Locate every Plasmodium parasite.
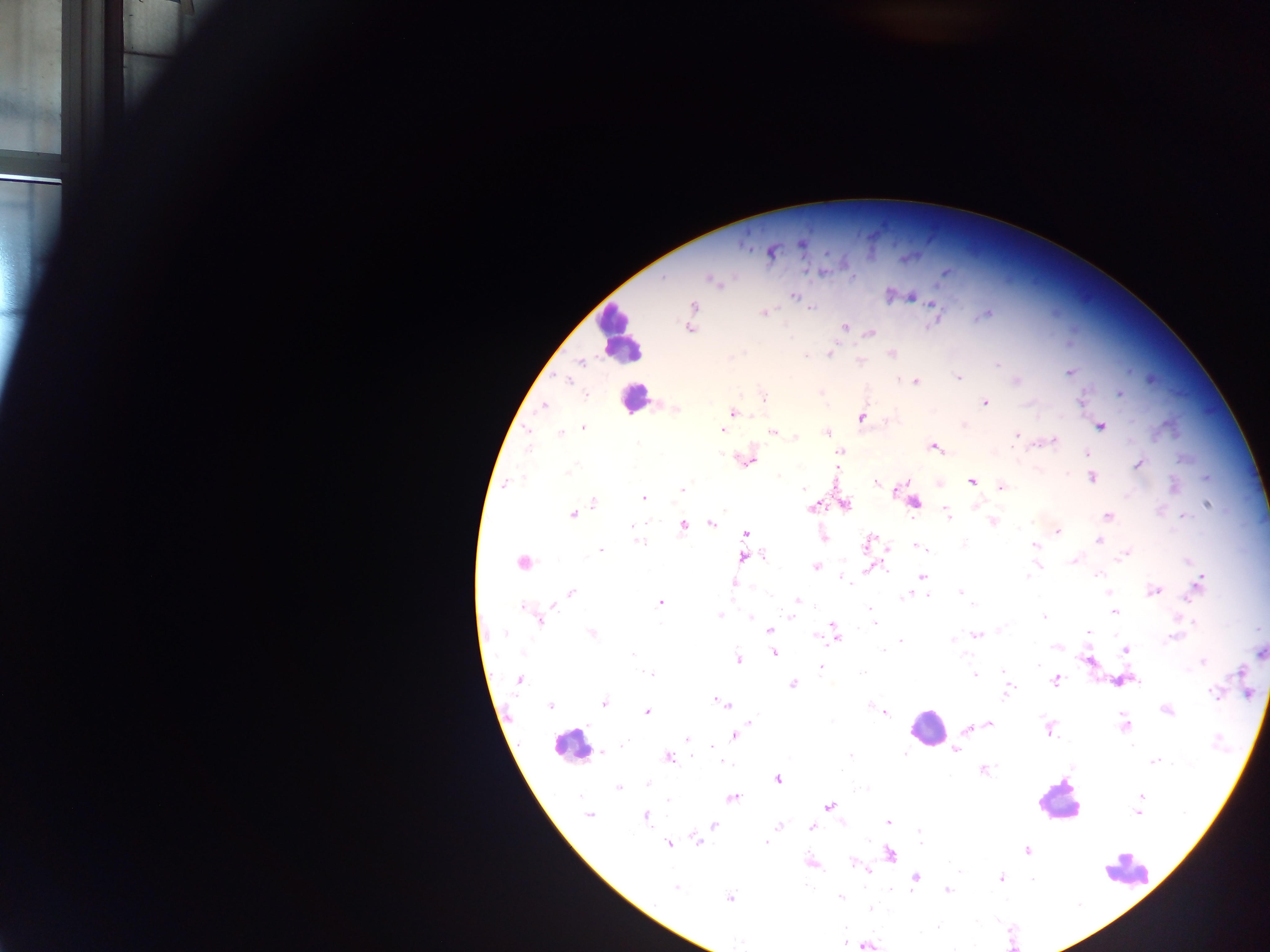

Approximate centers as x y in pixels.
Plasmodium parasites: 802 243; 772 252; 663 277; 712 281; 793 296; 911 297; 694 306; 810 308; 764 313; 985 314; 845 327; 689 328; 869 333; 830 353; 892 354; 805 355; 860 361; 580 363; 997 365; 1069 373; 958 378; 1150 379; 566 380; 1017 381; 916 382; 820 392; 1120 394; 585 395; 763 397; 986 403; 543 406; 676 409; 733 413; 861 418; 1100 426; 1167 427; 583 428; 723 429; 528 431; 773 432; 826 432; 561 433; 1017 435; 797 437; 1054 440; 529 446; 934 447; 840 452; 1087 453; 748 460; 1139 463; 569 471; 1092 477; 1207 477; 971 482; 876 483; 506 484; 1001 487; 681 489; 803 489; 644 498; 594 502; 915 502; 846 505; 1206 505; 812 508; 573 514; 947 515; 1108 515; 1183 516; 993 521; 712 523; 1026 524; 632 525; 683 525; 1058 532; 746 534; 824 537; 1099 540; 639 542; 868 543; 964 544; 918 546; 1034 546; 888 549; 601 550; 1124 555; 764 556; 743 558; 1075 560; 1189 562; 522 563; 816 567; 869 568; 1097 574; 1027 576; 923 577; 841 578; 1200 580; 845 581; 733 583; 1197 587; 1154 590; 960 591; 1108 592; 571 593; 770 595; 906 595; 925 596; 1189 598; 797 600; 660 603; 972 605; 552 606; 521 607; 869 608; 793 611; 1114 611; 719 616; 790 617; 1045 617; 751 618; 541 621; 1194 622; 875 624; 833 625; 1001 628; 769 630; 835 632; 1088 632; 505 634; 591 634; 976 634; 818 637; 1171 638; 952 640; 901 641; 1056 648; 883 650; 1125 651; 774 653; 1260 653; 523 654; 633 654; 962 654; 738 658; 1204 661; 1038 665; 821 668; 1003 670; 1187 670; 859 673; 650 674; 1239 674; 974 675; 519 679; 1056 681; 1137 681; 793 685; 1008 692; 1213 693; 1248 693; 604 703; 721 703; 870 704; 550 706; 1167 710; 647 712; 885 712; 750 722; 988 723; 1124 724; 967 728; 1049 730; 735 735; 687 739; 622 746; 711 747; 956 750; 602 752; 905 753; 850 755; 669 758; 724 762; 1154 762; 1073 767; 841 771; 983 771; 778 780; 647 783; 618 788; 580 797; 732 797; 1140 797; 668 800; 830 806; 1138 813; 588 816; 645 817; 888 822; 714 826; 778 826; 812 827; 919 832; 696 840; 765 842; 921 842; 669 843; 1027 850; 890 854; 852 862; 811 863; 867 870; 960 870; 1002 878; 916 879; 1032 880; 675 888; 895 890; 947 890; 841 897; 730 898; 870 909; 739 941; 845 942; 868 945.

Summary:
  - Leukocyte locations: 619 332; 634 399; 926 726; 570 746; 1056 801; 1128 871
  - Image size: 1270×952 pixels
  - Capture: mobile-phone photograph through a microscope
  - Country: Ghana
  - Field of view: single
  - Preparation: thick blood film